Name the parasite shown.
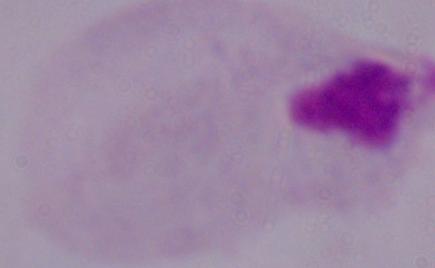
A trichomonad.

Summary:
  - Modality: micrograph
  - Magnification: 1000x